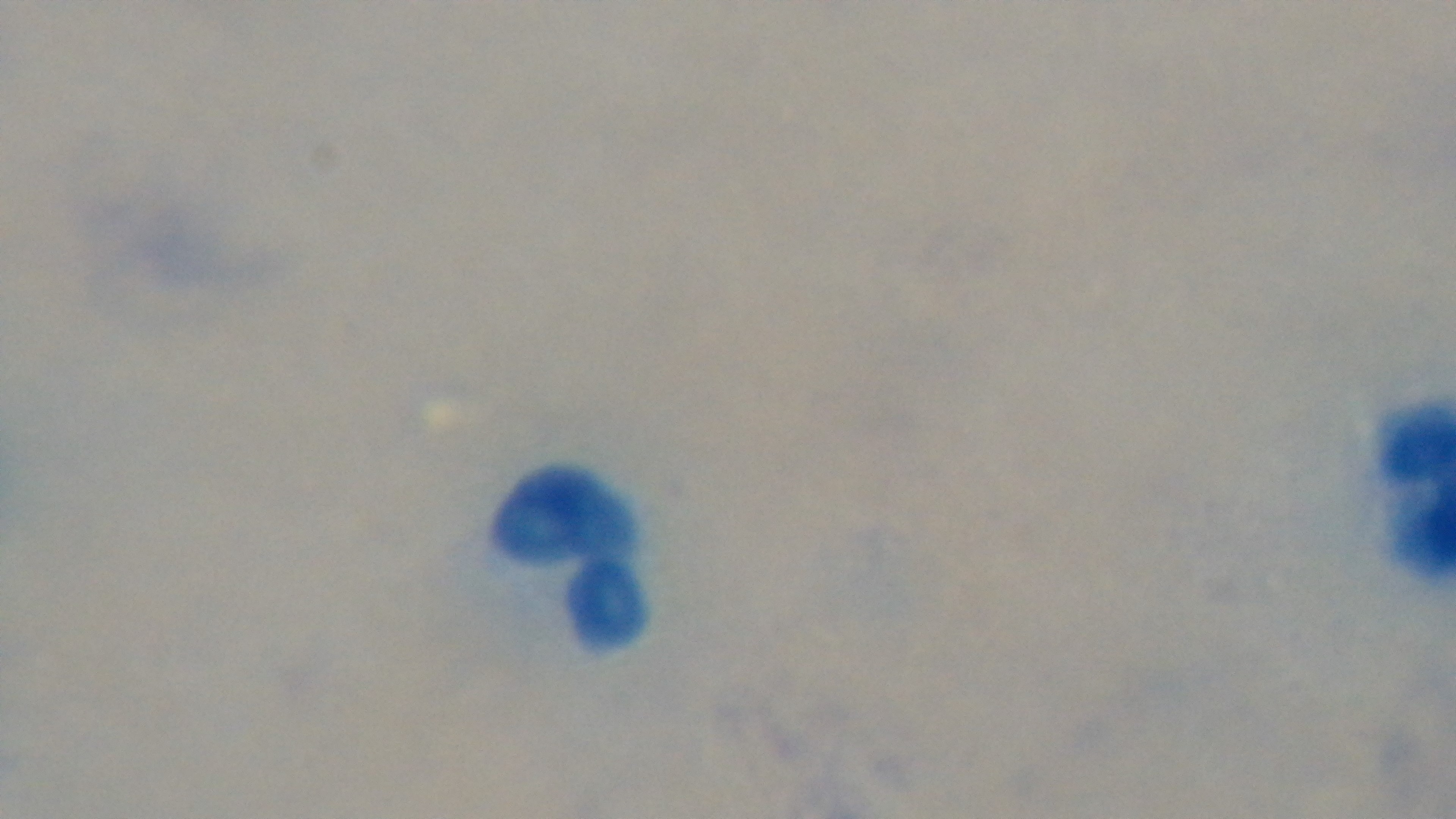
Giemsa stain. Preparation: thick. Light microscopy. Malaria status: negative. One field from the slide. Mounted 4K digital camera. Oil-immersion objective, 100x.